Point out each leukocyte.
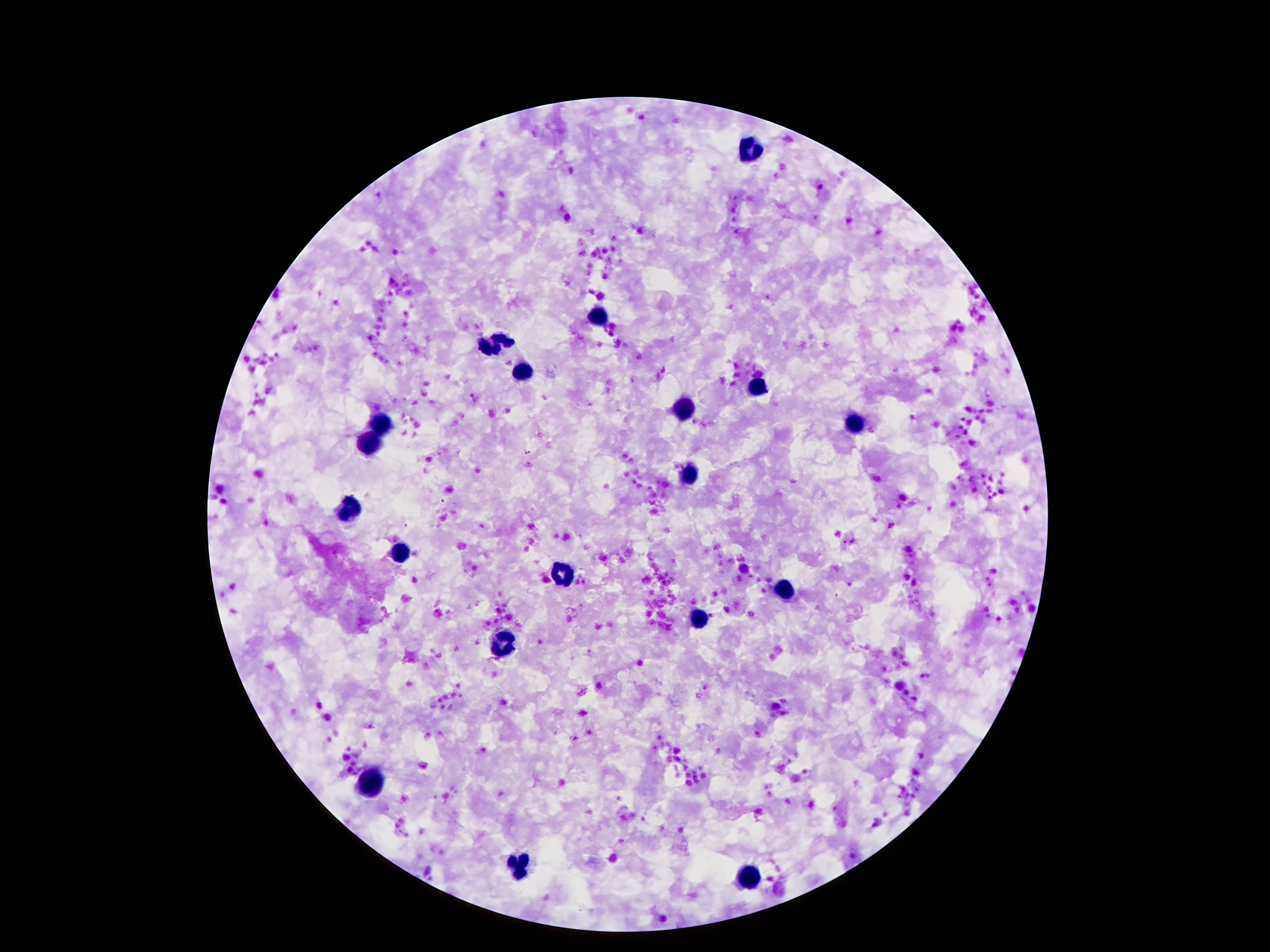

Approximate object centers, in pixels from the top-left corner.
Leukocytes: (x=749, y=151), (x=598, y=320), (x=493, y=344), (x=523, y=371), (x=762, y=387), (x=687, y=406), (x=855, y=421), (x=381, y=424), (x=368, y=445), (x=689, y=475), (x=351, y=508), (x=400, y=551), (x=562, y=574), (x=786, y=587), (x=698, y=620), (x=499, y=648), (x=372, y=781), (x=517, y=865), (x=751, y=875).

One field from this slide. Image is 1270×952 pixels. Giemsa-stained preparation. 100x magnification. Patient malaria status: negative. Smartphone photograph taken through the microscope eyepiece. Thick blood smear.